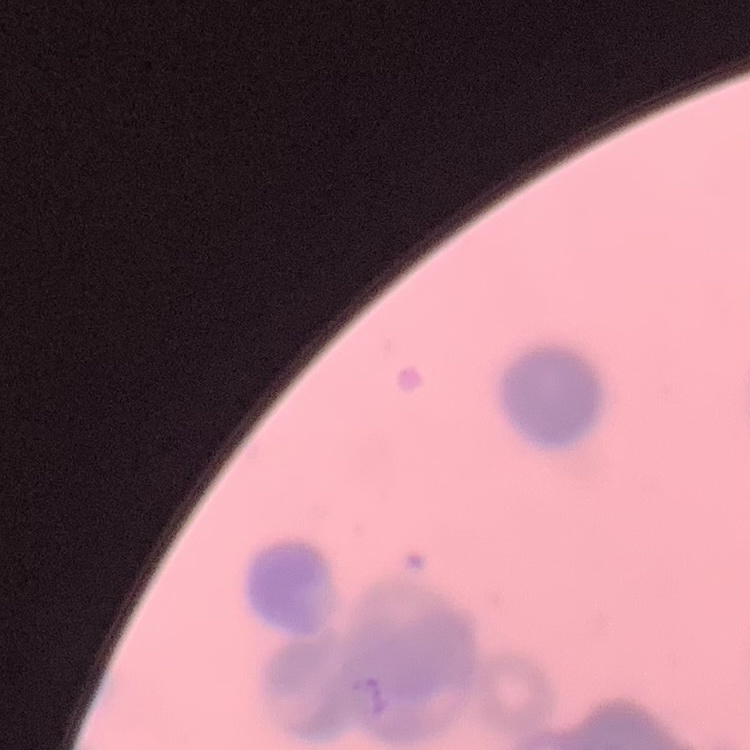

Summary:
  - Erythrocyte morphology: rouleaux formation
  - Stain: Field's or Giemsa
  - Image type: one tile cut from a larger photomicrograph
  - Preparation: thin peripheral smear